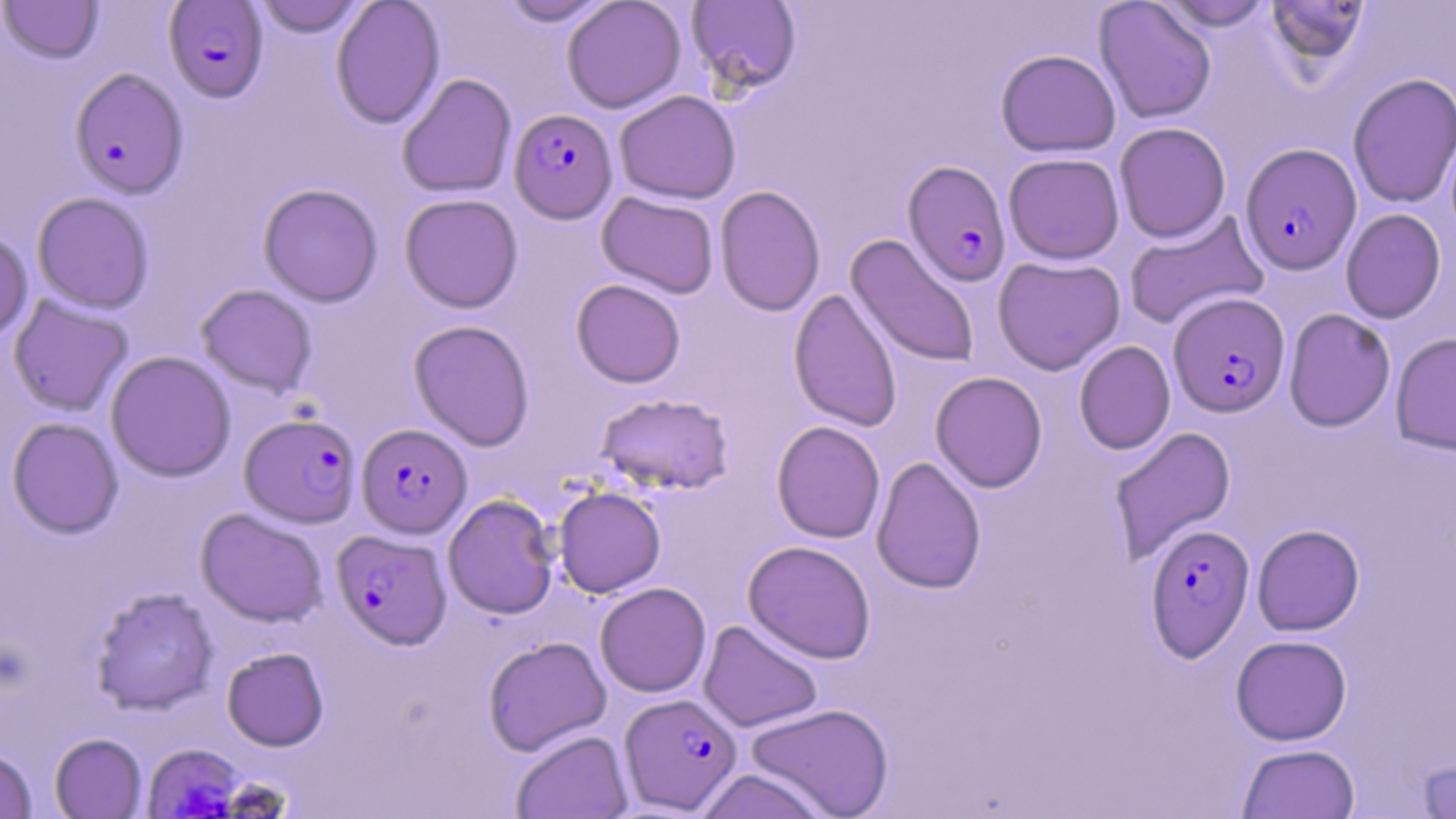

slide-level diagnosis = Plasmodium falciparum
magnification = 1000x
uninfected red blood cell locations = approximate bounding boxes as [x1, y1, x2, y2] in pixels: [0, 0, 104, 64], [251, 0, 370, 37], [330, 0, 445, 129], [495, 0, 616, 27], [561, 0, 686, 113], [1265, 0, 1369, 69], [686, 1, 802, 96], [1094, 1, 1217, 123], [1152, 1, 1278, 32], [995, 49, 1121, 157], [396, 73, 517, 198], [1348, 73, 1456, 209], [614, 90, 741, 204], [1114, 122, 1231, 243], [1003, 152, 1125, 264], [258, 183, 383, 307], [714, 185, 826, 317], [597, 191, 719, 298], [31, 192, 155, 313], [400, 193, 523, 313], [1341, 208, 1447, 324], [1123, 210, 1270, 330], [0, 227, 33, 344], [846, 234, 981, 368], [992, 255, 1125, 375], [571, 279, 686, 388], [195, 284, 318, 398], [788, 288, 903, 432], [7, 295, 134, 417], [1283, 308, 1396, 432], [409, 319, 535, 451], [1390, 332, 1456, 456], [1074, 340, 1175, 455], [105, 351, 236, 482], [930, 371, 1048, 493], [595, 392, 735, 495], [6, 417, 124, 538], [771, 421, 886, 544], [1108, 426, 1237, 565], [871, 456, 986, 594], [553, 486, 666, 597], [443, 494, 559, 619], [195, 508, 328, 627], [1252, 524, 1365, 635], [743, 540, 876, 663], [595, 582, 711, 697], [90, 587, 219, 716], [698, 620, 823, 732], [1230, 635, 1352, 745], [482, 636, 612, 756], [222, 647, 329, 751], [745, 703, 895, 819], [511, 730, 633, 819], [49, 733, 147, 818], [1237, 743, 1360, 818], [0, 748, 36, 817], [1415, 757, 1456, 818], [696, 768, 829, 819]
Plasmodium falciparum-infected red blood cell locations = approximate bounding boxes as [x1, y1, x2, y2] in pixels: [163, 1, 269, 103], [69, 67, 188, 198], [509, 108, 617, 223], [1240, 143, 1361, 275], [902, 160, 1011, 287], [1168, 292, 1290, 417], [240, 412, 361, 528], [357, 423, 472, 538], [1145, 523, 1255, 662], [333, 529, 451, 649], [619, 693, 742, 814], [142, 744, 244, 819]
stain = May-Grünwald-Giemsa
image size = 1456×819 pixels
field of view = single
preparation = thin blood smear
modality = optical microscopy